State which parasite is depicted.
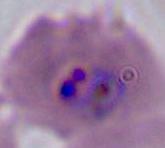

Plasmodium.

Summary:
  - Modality: photomicrograph
  - Magnification: 400x or 1000x